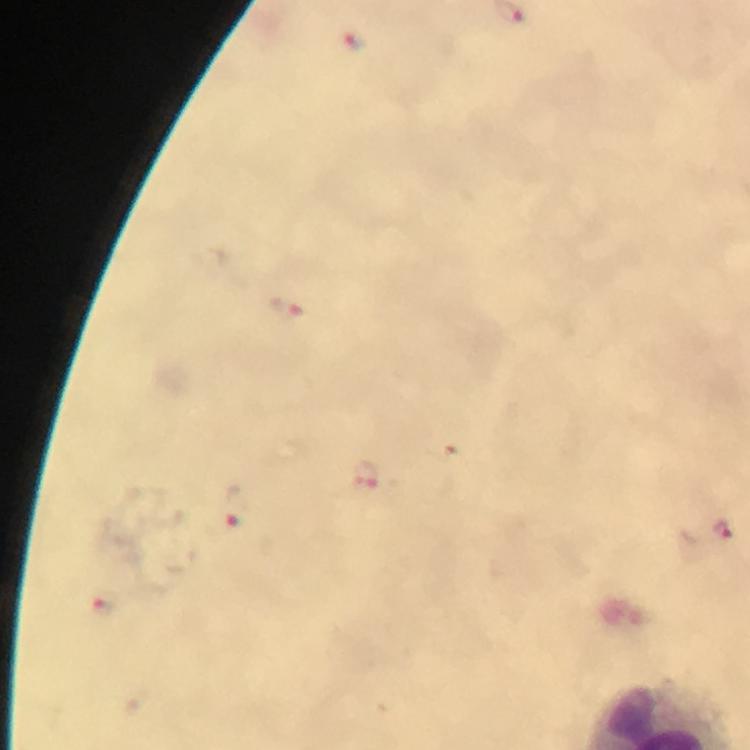 Approximate centers as [x, y] in pixels. Plasmodium parasite locations: [354, 43], [285, 307], [363, 474], [235, 507], [723, 529], [108, 606]. Image is 750×750 pixels. Giemsa stain. Immersion oil applied. 100x magnification. Photographed with a smartphone mounted on the microscope. Cropped region of a single field of view. Thick smear. From a diagnostic examination for malaria.